State the preparation type.
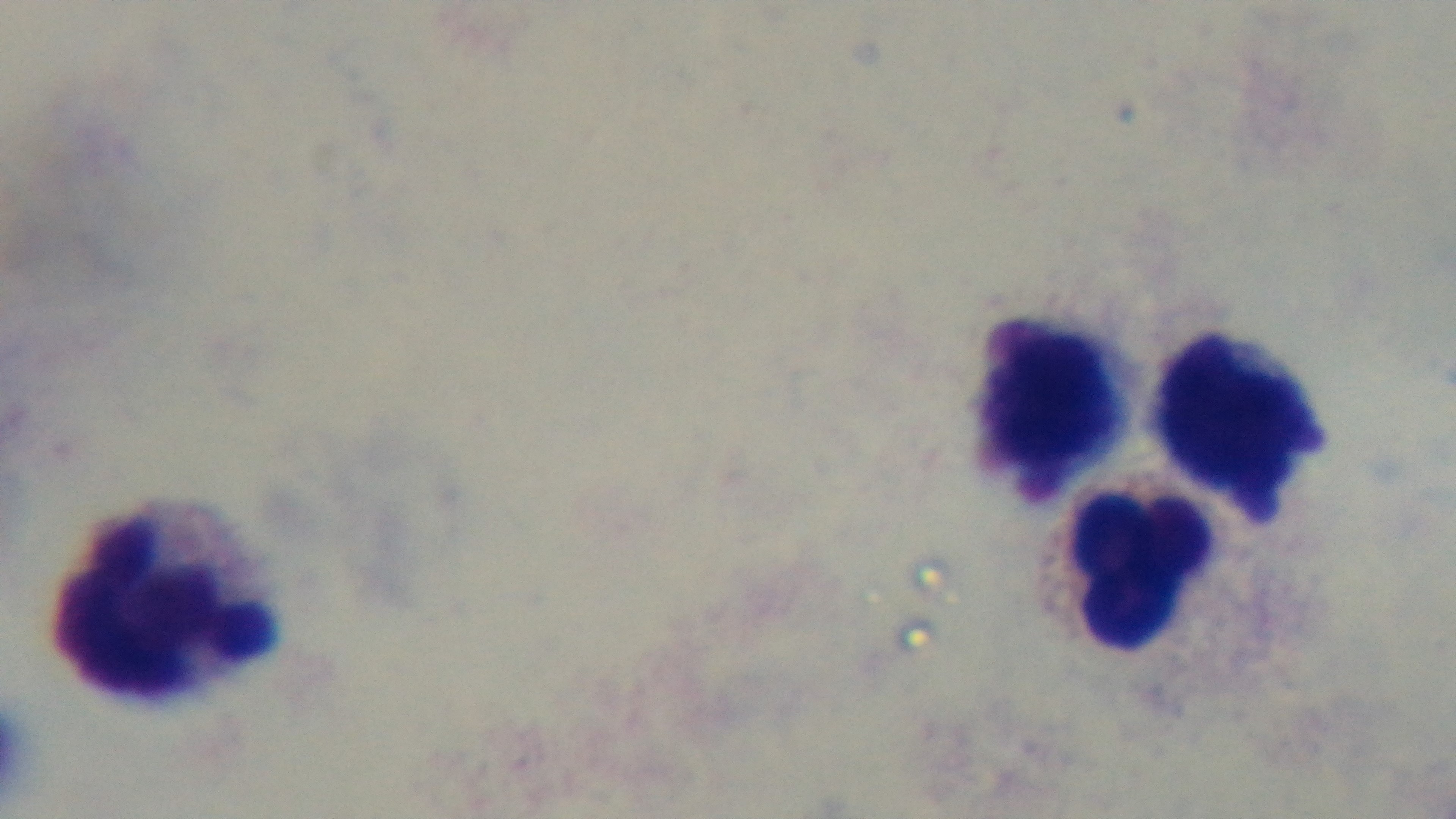
It is a thick blood film.

Captured with a mounted 4K digital camera. Single field of view. Light microscopy. 100x oil-immersion objective. Malaria status: negative. Giemsa-stained.